State which parasite is depicted.
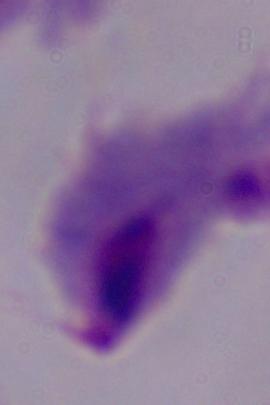
A trichomonad.

Captured at 1000x magnification. Micrograph.